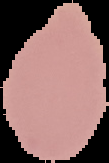
image_size: 109×163 pixels
preparation: thin blood film
image_type: segmented cell region on a black background
result: no Plasmodium parasites seen